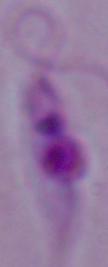

Summary:
  - Identification: Leishmania
  - Magnification: 1000x
  - Modality: photomicrograph